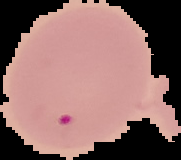
Summary:
  - Preparation: thin blood film
  - Image type: segmented cell region on a black background
  - Result: Plasmodium parasites identified
  - Image size: 181×160 pixels